Name the parasite shown.
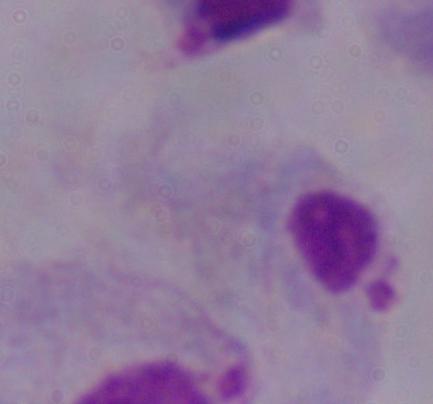
A trichomonad.

Captured at 1000x magnification. Photomicrograph.